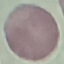
{
  "malaria_status": "uninfected",
  "stain": "Giemsa",
  "image_type": "cell patch, automatically extracted from a larger field of view and resized to 64 × 64 pixels",
  "preparation": "thin blood smear",
  "capture": "smartphone through the microscope eyepiece"
}